Point out each Plasmodium parasite.
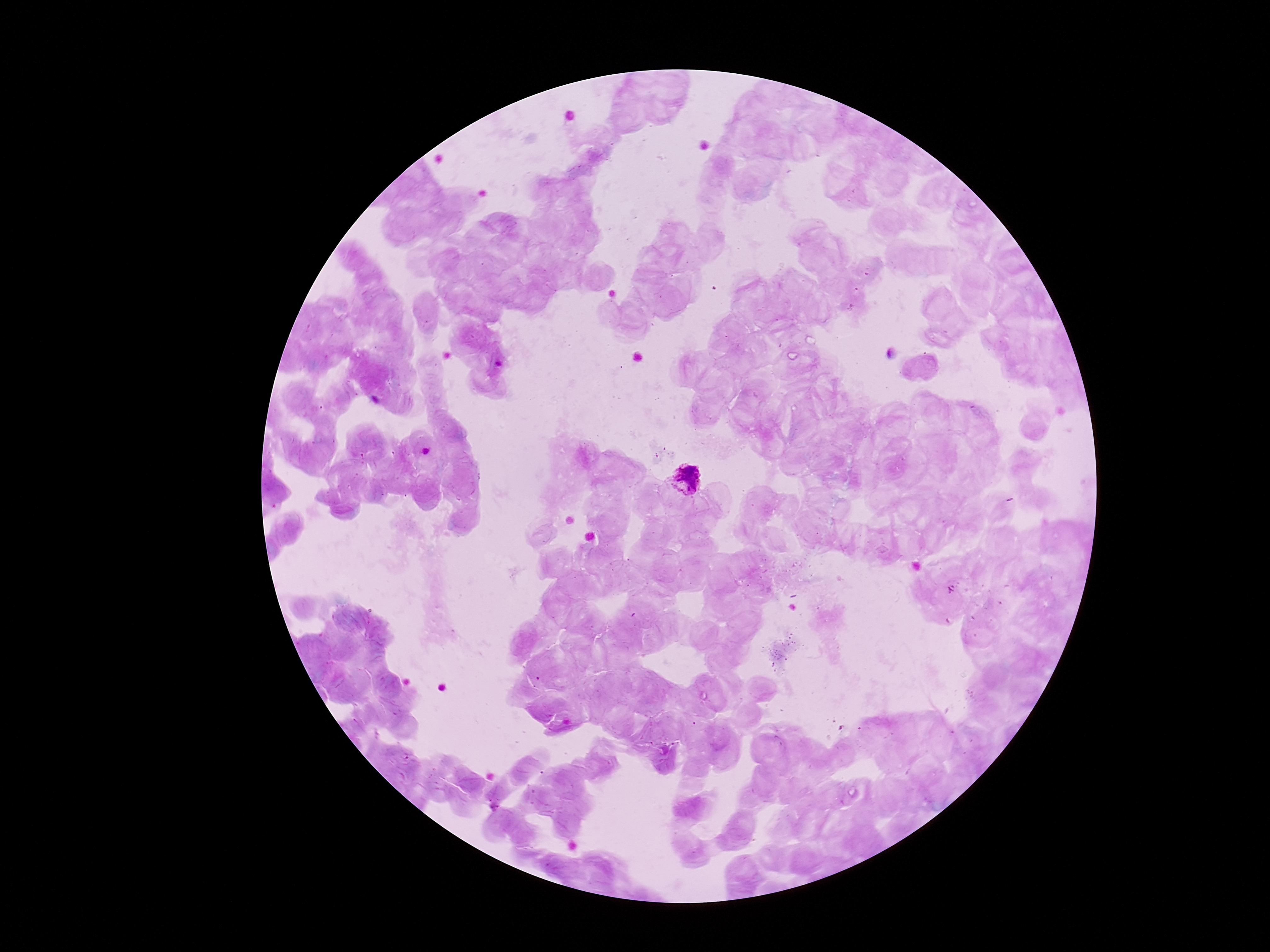

Approximate centers as [x, y] in pixels.
Plasmodium parasites: [686, 478].

preparation = thick peripheral-blood smear
magnification = 100x
field of view = single
capture = smartphone camera through the microscope eyepiece
stain = Giemsa
patient malaria status = positive
image size = 1270×952 pixels